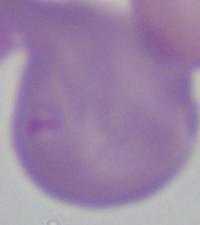

Photomicrograph. 1000x magnification. A Babesia parasite is shown.